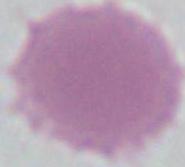

1000x magnification. Micrograph. An erythrocyte is seen.